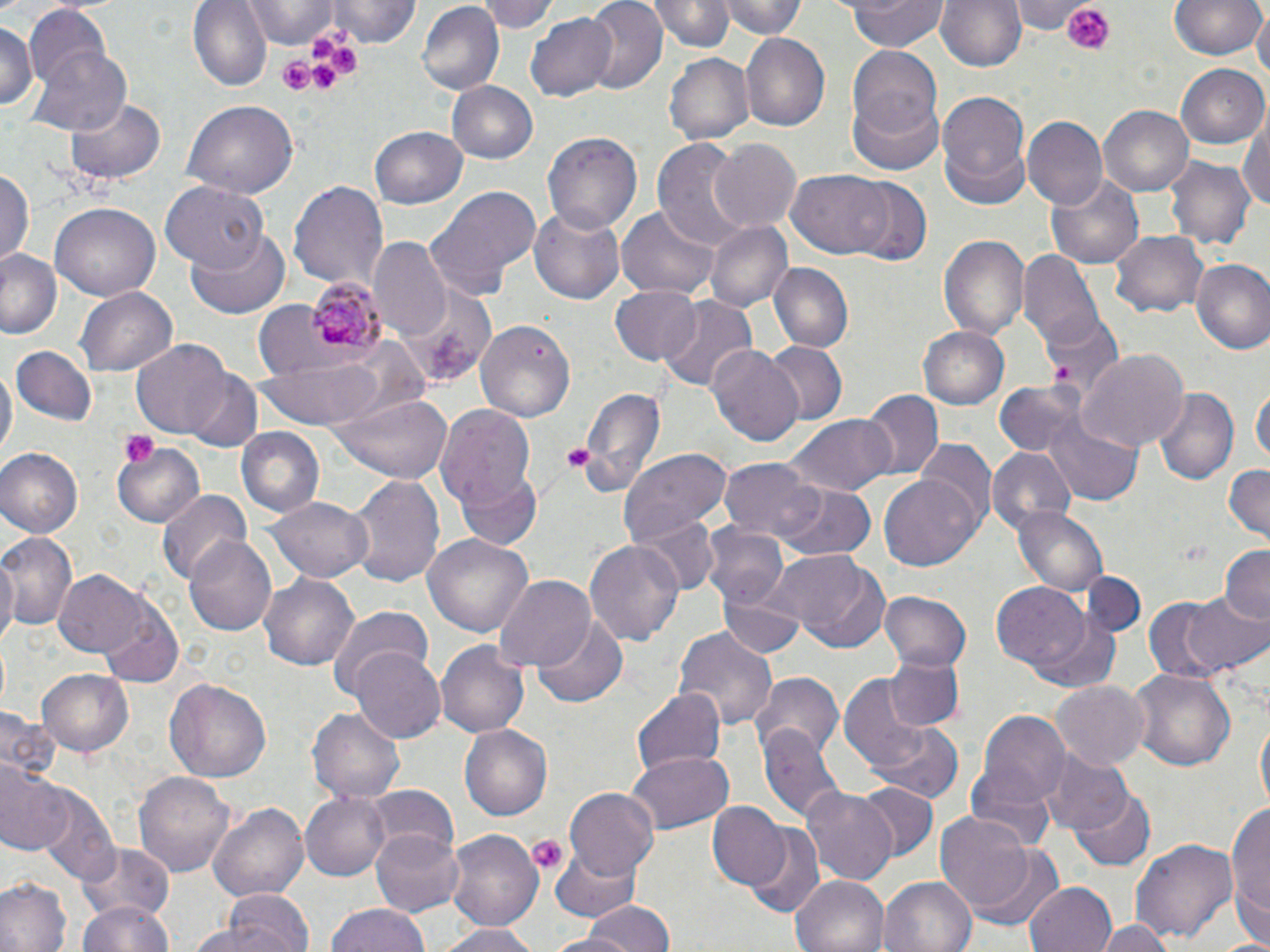

slide_level_diagnosis: Plasmodium malariae
field_of_view: single
platelet_locations: 'approximate bounding boxes as named x1/y1/x2/y2 corners in pixels: (x1=1060, y1=0, x2=1118, y2=54), (x1=308, y1=35, x2=336, y2=62), (x1=330, y1=47, x2=360, y2=76), (x1=281, y1=57, x2=315, y2=92), (x1=312, y1=60, x2=337, y2=90), (x1=117, y1=431, x2=159, y2=470), (x1=560, y1=445, x2=593, y2=474), (x1=528, y1=835, x2=567, y2=875)'
magnification: 1000x
uninfected_red_blood_cell_locations: 'approximate bounding boxes as named x1/y1/x2/y2 corners in pixels: (x1=188, y1=0, x2=272, y2=92), (x1=330, y1=0, x2=420, y2=48), (x1=479, y1=0, x2=559, y2=33), (x1=583, y1=0, x2=667, y2=93), (x1=651, y1=0, x2=734, y2=53), (x1=723, y1=0, x2=805, y2=40), (x1=843, y1=0, x2=947, y2=51), (x1=935, y1=0, x2=1027, y2=75), (x1=1015, y1=0, x2=1088, y2=33), (x1=1169, y1=0, x2=1265, y2=62), (x1=243, y1=1, x2=339, y2=45), (x1=416, y1=3, x2=505, y2=95), (x1=24, y1=5, x2=115, y2=97), (x1=1253, y1=9, x2=1269, y2=85), (x1=527, y1=11, x2=619, y2=102), (x1=0, y1=20, x2=38, y2=116), (x1=740, y1=32, x2=829, y2=132), (x1=29, y1=41, x2=133, y2=137), (x1=846, y1=43, x2=943, y2=144), (x1=665, y1=52, x2=755, y2=146), (x1=1178, y1=65, x2=1270, y2=150), (x1=447, y1=81, x2=537, y2=165), (x1=936, y1=90, x2=1031, y2=207), (x1=846, y1=93, x2=946, y2=175), (x1=65, y1=96, x2=169, y2=186), (x1=183, y1=100, x2=298, y2=198), (x1=1100, y1=105, x2=1193, y2=196), (x1=1242, y1=112, x2=1270, y2=216), (x1=1025, y1=116, x2=1108, y2=210), (x1=370, y1=126, x2=467, y2=211), (x1=544, y1=130, x2=641, y2=233), (x1=653, y1=136, x2=756, y2=255), (x1=709, y1=139, x2=801, y2=234), (x1=1168, y1=157, x2=1255, y2=251), (x1=0, y1=165, x2=35, y2=269), (x1=789, y1=168, x2=893, y2=259), (x1=1043, y1=170, x2=1146, y2=271), (x1=846, y1=177, x2=932, y2=267), (x1=289, y1=180, x2=389, y2=291), (x1=163, y1=181, x2=267, y2=274), (x1=425, y1=185, x2=541, y2=301), (x1=50, y1=202, x2=158, y2=303), (x1=616, y1=205, x2=717, y2=299), (x1=528, y1=207, x2=628, y2=304), (x1=706, y1=220, x2=792, y2=313), (x1=187, y1=224, x2=290, y2=318), (x1=937, y1=231, x2=1030, y2=340), (x1=1111, y1=231, x2=1210, y2=317), (x1=369, y1=240, x2=452, y2=341), (x1=0, y1=249, x2=62, y2=340), (x1=1019, y1=251, x2=1102, y2=346), (x1=1189, y1=260, x2=1270, y2=356), (x1=769, y1=263, x2=853, y2=352), (x1=395, y1=280, x2=495, y2=385), (x1=610, y1=283, x2=703, y2=363), (x1=76, y1=288, x2=175, y2=374), (x1=658, y1=296, x2=758, y2=396), (x1=1038, y1=310, x2=1123, y2=401), (x1=477, y1=319, x2=576, y2=422), (x1=918, y1=326, x2=1009, y2=411), (x1=133, y1=341, x2=232, y2=438), (x1=763, y1=343, x2=846, y2=423), (x1=14, y1=345, x2=96, y2=425), (x1=708, y1=345, x2=805, y2=448), (x1=1078, y1=350, x2=1186, y2=455), (x1=258, y1=355, x2=393, y2=427), (x1=0, y1=364, x2=15, y2=461), (x1=186, y1=368, x2=263, y2=453), (x1=995, y1=381, x2=1084, y2=458), (x1=578, y1=383, x2=666, y2=497), (x1=1253, y1=386, x2=1269, y2=469), (x1=1153, y1=388, x2=1237, y2=488), (x1=331, y1=390, x2=453, y2=484), (x1=860, y1=391, x2=942, y2=481), (x1=436, y1=403, x2=536, y2=508), (x1=1042, y1=408, x2=1143, y2=508), (x1=784, y1=416, x2=895, y2=496), (x1=234, y1=427, x2=325, y2=520), (x1=111, y1=441, x2=205, y2=529), (x1=917, y1=441, x2=997, y2=533), (x1=620, y1=446, x2=731, y2=546), (x1=0, y1=447, x2=82, y2=537), (x1=987, y1=447, x2=1076, y2=534), (x1=721, y1=456, x2=819, y2=542), (x1=1223, y1=464, x2=1269, y2=542), (x1=879, y1=471, x2=981, y2=569), (x1=455, y1=473, x2=543, y2=553), (x1=347, y1=474, x2=445, y2=588), (x1=777, y1=484, x2=876, y2=564), (x1=156, y1=489, x2=253, y2=585), (x1=267, y1=494, x2=373, y2=584), (x1=1013, y1=506, x2=1108, y2=596), (x1=628, y1=509, x2=723, y2=597), (x1=700, y1=523, x2=788, y2=609), (x1=0, y1=531, x2=79, y2=634), (x1=423, y1=533, x2=533, y2=637), (x1=183, y1=534, x2=277, y2=636), (x1=583, y1=537, x2=686, y2=647), (x1=0, y1=545, x2=18, y2=651), (x1=1219, y1=545, x2=1270, y2=622), (x1=769, y1=549, x2=889, y2=652), (x1=54, y1=569, x2=150, y2=659), (x1=260, y1=570, x2=359, y2=670), (x1=1078, y1=570, x2=1150, y2=637), (x1=493, y1=576, x2=597, y2=673), (x1=993, y1=583, x2=1091, y2=671), (x1=881, y1=590, x2=971, y2=673), (x1=1182, y1=591, x2=1270, y2=675), (x1=717, y1=592, x2=807, y2=658), (x1=1142, y1=596, x2=1236, y2=686), (x1=97, y1=598, x2=185, y2=685), (x1=325, y1=604, x2=433, y2=701), (x1=1029, y1=614, x2=1119, y2=693), (x1=532, y1=617, x2=627, y2=709), (x1=674, y1=624, x2=778, y2=732), (x1=437, y1=641, x2=528, y2=738), (x1=350, y1=648, x2=446, y2=744), (x1=883, y1=654, x2=966, y2=730), (x1=1129, y1=667, x2=1234, y2=771), (x1=38, y1=669, x2=134, y2=756), (x1=750, y1=671, x2=843, y2=759), (x1=837, y1=672, x2=935, y2=774), (x1=163, y1=678, x2=270, y2=782), (x1=1052, y1=679, x2=1149, y2=771), (x1=631, y1=690, x2=725, y2=776), (x1=308, y1=705, x2=406, y2=804), (x1=970, y1=706, x2=1072, y2=819), (x1=0, y1=710, x2=62, y2=782), (x1=1253, y1=714, x2=1268, y2=820), (x1=460, y1=724, x2=554, y2=821), (x1=869, y1=724, x2=962, y2=798), (x1=759, y1=725, x2=846, y2=823), (x1=1043, y1=749, x2=1131, y2=836), (x1=627, y1=751, x2=734, y2=836), (x1=0, y1=759, x2=66, y2=855), (x1=134, y1=769, x2=236, y2=878), (x1=362, y1=783, x2=458, y2=862), (x1=856, y1=783, x2=937, y2=861), (x1=33, y1=785, x2=118, y2=882), (x1=565, y1=787, x2=659, y2=883), (x1=802, y1=787, x2=899, y2=887), (x1=1071, y1=789, x2=1155, y2=871), (x1=300, y1=791, x2=391, y2=880), (x1=1227, y1=796, x2=1270, y2=940), (x1=210, y1=801, x2=308, y2=904), (x1=710, y1=802, x2=789, y2=889), (x1=934, y1=811, x2=1041, y2=915), (x1=370, y1=825, x2=465, y2=914), (x1=746, y1=825, x2=825, y2=919), (x1=448, y1=829, x2=544, y2=929), (x1=1130, y1=836, x2=1238, y2=945), (x1=959, y1=840, x2=1067, y2=934), (x1=549, y1=842, x2=641, y2=923), (x1=79, y1=845, x2=176, y2=926), (x1=792, y1=875, x2=891, y2=952), (x1=880, y1=876, x2=975, y2=952), (x1=0, y1=878, x2=72, y2=952), (x1=1024, y1=881, x2=1119, y2=952), (x1=217, y1=889, x2=316, y2=952), (x1=568, y1=898, x2=674, y2=952), (x1=74, y1=900, x2=178, y2=952), (x1=325, y1=904, x2=432, y2=952), (x1=1098, y1=917, x2=1175, y2=952), (x1=438, y1=922, x2=540, y2=952)'
plasmodium_malariae_infected_red_blood_cell_locations: 'approximate bounding boxes as named x1/y1/x2/y2 corners in pixels: (x1=302, y1=276, x2=386, y2=359)'
preparation: thin blood film
stain: May-Grünwald-Giemsa
modality: light microscopy
image_size: 1270×952 pixels